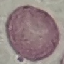
Summary:
  - Malaria status: uninfected
  - Preparation: thin smear
  - Capture: smartphone through the microscope eyepiece
  - Stain: Giemsa
  - Image type: cell patch, automatically extracted from a larger field of view and resized to 64 × 64 pixels